Classify this cell by malaria status.
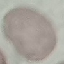

Uninfected.

{
  "capture": "smartphone through the microscope eyepiece",
  "preparation": "thin blood smear",
  "stain": "Giemsa",
  "image_type": "cell patch, automatically extracted from a larger field of view and resized to 64 × 64 pixels"
}